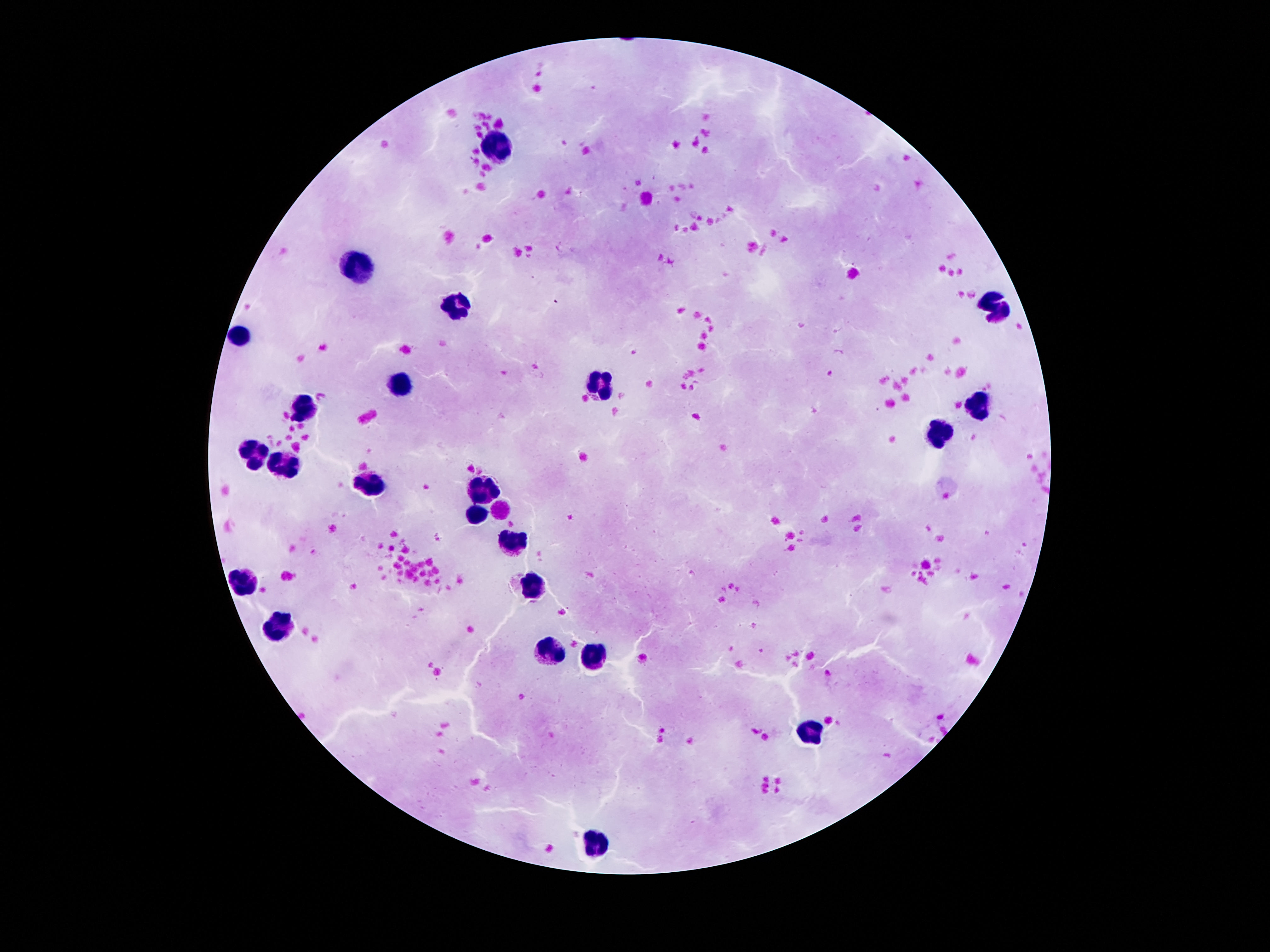

magnification = 100x
capture = smartphone camera through the microscope eyepiece
leukocyte locations = approximate centers as {x, y} in pixels: {498, 145}, {358, 267}, {458, 305}, {999, 306}, {239, 333}, {605, 383}, {404, 384}, {979, 407}, {303, 408}, {936, 435}, {254, 456}, {285, 462}, {364, 482}, {486, 491}, {476, 511}, {512, 542}, {244, 581}, {532, 586}, {280, 623}, {549, 651}, {593, 655}, {809, 731}, {598, 843}
patient malaria status = not infected
field of view = single
preparation = thick blood smear
stain = Giemsa
image size = 1270×952 pixels